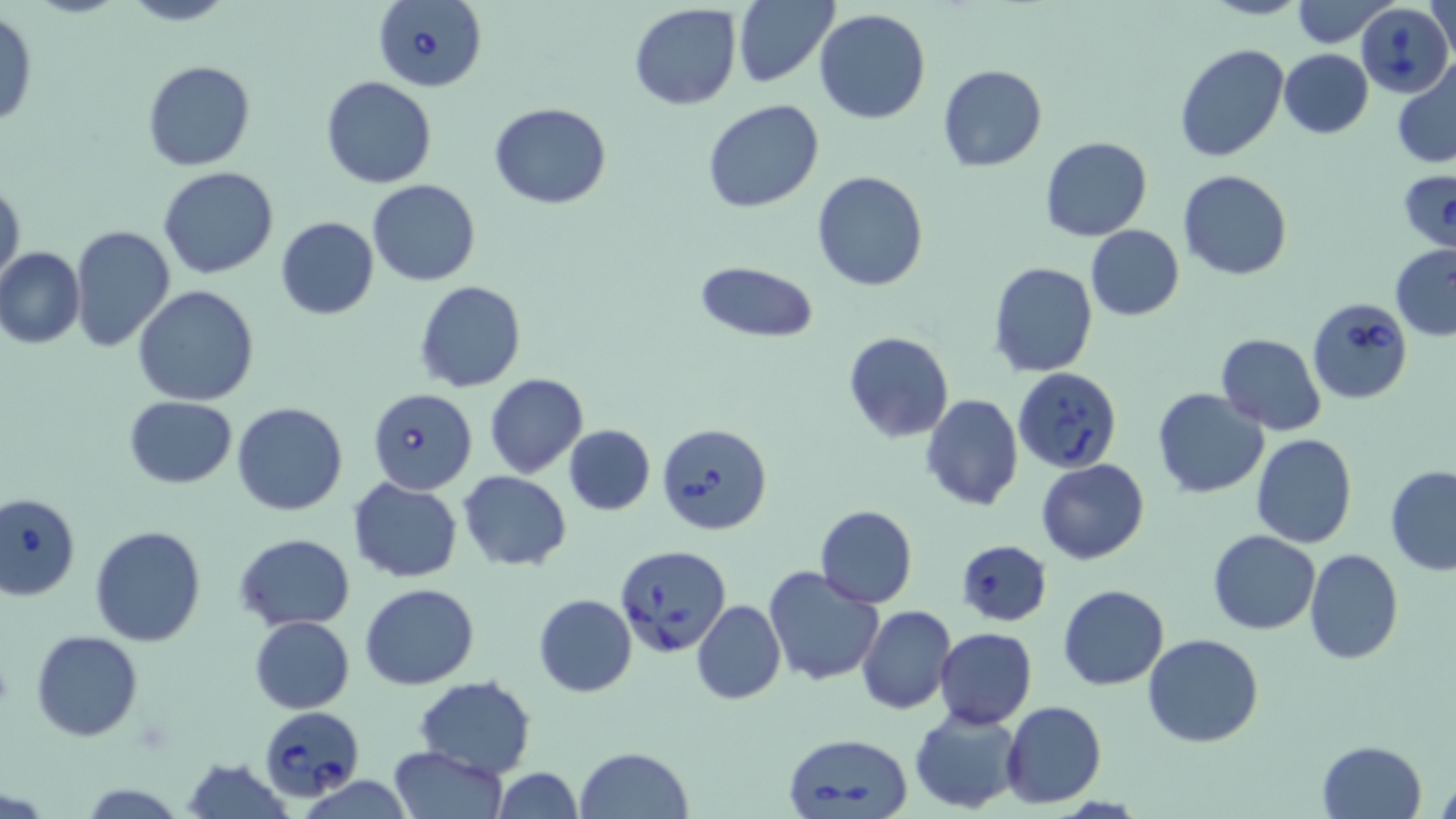

Summary:
  - Coordinate format: approximate bounding boxes as named x1/y1/x2/y2 corners in pixels
  - Babesia divergens-infected red blood cell locations: (x1=374, y1=0, x2=488, y2=93), (x1=1355, y1=1, x2=1453, y2=98), (x1=1398, y1=169, x2=1456, y2=256), (x1=1307, y1=298, x2=1413, y2=404), (x1=1011, y1=365, x2=1124, y2=473), (x1=368, y1=388, x2=477, y2=495), (x1=659, y1=422, x2=774, y2=535), (x1=1, y1=491, x2=80, y2=601), (x1=614, y1=545, x2=731, y2=660), (x1=257, y1=710, x2=365, y2=805), (x1=783, y1=732, x2=914, y2=819)
  - Uninfected red blood cell locations: (x1=116, y1=0, x2=239, y2=27), (x1=1201, y1=0, x2=1308, y2=20), (x1=1292, y1=0, x2=1394, y2=47), (x1=733, y1=1, x2=838, y2=88), (x1=1426, y1=1, x2=1456, y2=57), (x1=628, y1=3, x2=742, y2=111), (x1=814, y1=9, x2=930, y2=124), (x1=0, y1=11, x2=38, y2=128), (x1=1174, y1=44, x2=1290, y2=164), (x1=1279, y1=49, x2=1373, y2=139), (x1=141, y1=61, x2=256, y2=171), (x1=1392, y1=63, x2=1456, y2=167), (x1=939, y1=64, x2=1047, y2=172), (x1=320, y1=76, x2=438, y2=189), (x1=702, y1=99, x2=825, y2=212), (x1=488, y1=101, x2=612, y2=209), (x1=1040, y1=137, x2=1153, y2=241), (x1=157, y1=167, x2=279, y2=280), (x1=1177, y1=169, x2=1292, y2=279), (x1=811, y1=171, x2=929, y2=293), (x1=0, y1=179, x2=24, y2=288), (x1=367, y1=180, x2=479, y2=287), (x1=275, y1=216, x2=380, y2=320), (x1=1084, y1=224, x2=1184, y2=321), (x1=69, y1=225, x2=176, y2=354), (x1=1389, y1=242, x2=1456, y2=341), (x1=0, y1=247, x2=85, y2=348), (x1=988, y1=261, x2=1098, y2=379), (x1=695, y1=262, x2=818, y2=342), (x1=414, y1=281, x2=525, y2=392), (x1=134, y1=285, x2=258, y2=405), (x1=842, y1=330, x2=954, y2=442), (x1=1214, y1=333, x2=1325, y2=435), (x1=485, y1=374, x2=587, y2=476), (x1=1152, y1=388, x2=1269, y2=497), (x1=920, y1=394, x2=1023, y2=511), (x1=124, y1=396, x2=237, y2=488), (x1=231, y1=402, x2=347, y2=516), (x1=1172, y1=420, x2=1326, y2=533), (x1=563, y1=424, x2=656, y2=515), (x1=1251, y1=433, x2=1358, y2=549), (x1=1036, y1=460, x2=1149, y2=565), (x1=1385, y1=465, x2=1456, y2=577), (x1=459, y1=471, x2=572, y2=570), (x1=347, y1=476, x2=464, y2=583), (x1=814, y1=505, x2=917, y2=608), (x1=89, y1=525, x2=206, y2=647), (x1=1208, y1=529, x2=1320, y2=635), (x1=234, y1=533, x2=355, y2=632), (x1=956, y1=537, x2=1050, y2=626), (x1=1304, y1=548, x2=1403, y2=664), (x1=762, y1=565, x2=885, y2=686), (x1=360, y1=583, x2=480, y2=690), (x1=1058, y1=584, x2=1170, y2=691), (x1=534, y1=593, x2=637, y2=696), (x1=692, y1=600, x2=786, y2=704), (x1=857, y1=606, x2=954, y2=715), (x1=248, y1=615, x2=355, y2=712), (x1=935, y1=627, x2=1037, y2=729), (x1=30, y1=630, x2=145, y2=741), (x1=1142, y1=634, x2=1264, y2=748), (x1=414, y1=676, x2=537, y2=778), (x1=1000, y1=700, x2=1107, y2=810), (x1=909, y1=707, x2=1026, y2=814), (x1=1316, y1=740, x2=1426, y2=818), (x1=389, y1=746, x2=507, y2=819), (x1=574, y1=746, x2=693, y2=819), (x1=183, y1=757, x2=294, y2=819), (x1=489, y1=767, x2=585, y2=819), (x1=1435, y1=776, x2=1456, y2=818), (x1=75, y1=782, x2=192, y2=818)
  - Slide-level diagnosis: Babesia divergens
  - Preparation: thin blood film
  - Stain: May-Grünwald-Giemsa
  - Field of view: single
  - Magnification: 1000x
  - Image size: 1456×819 pixels
  - Modality: light microscopy